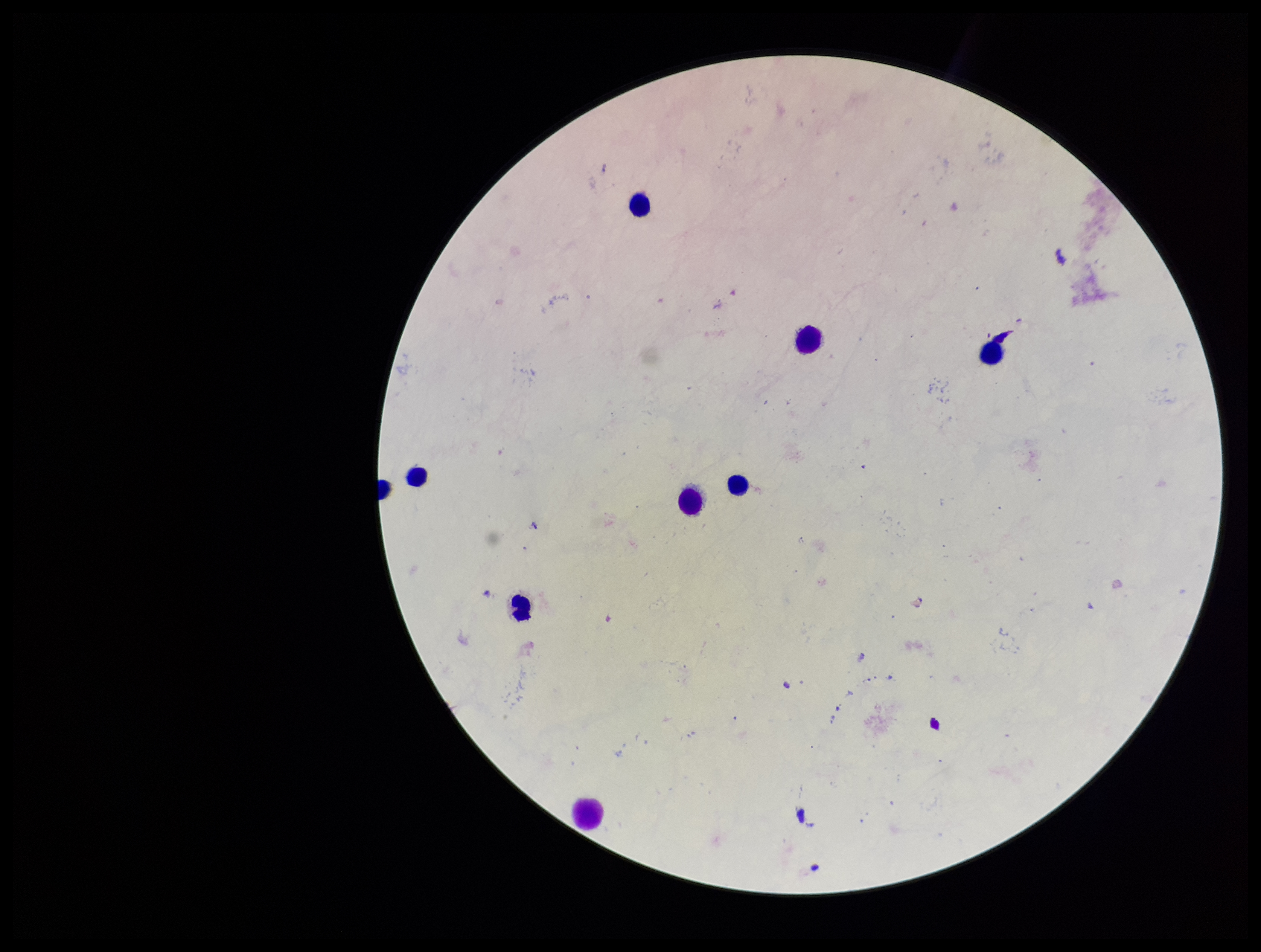
stain = Giemsa
field of view = single
preparation = thick blood smear
image size = 1261×952 pixels
parasite count = 0
Plasmodium parasites = none detected
capture = smartphone photograph through the microscope eyepiece
patient malaria status = negative
leukocyte count = 9